Name the parasite shown.
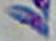

This is Toxoplasma gondii.

1000x magnification. Photomicrograph.